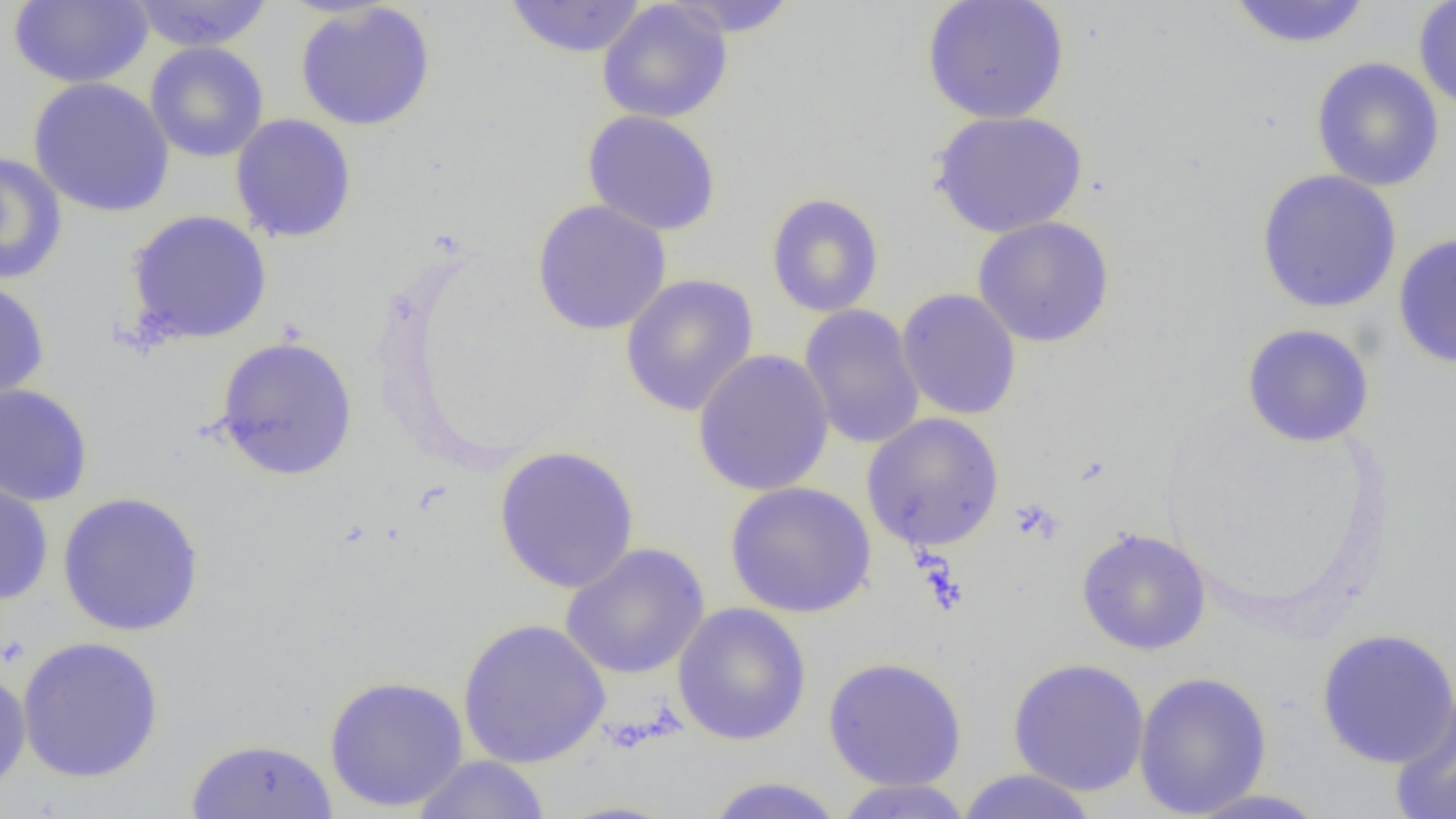

Summary:
  - Coordinate format: approximate bounding boxes as named x1/y1/x2/y2 corners in pixels
  - Platelet locations: (x1=1009, y1=498, x2=1064, y2=544)
  - Uninfected red blood cell locations: (x1=128, y1=0, x2=275, y2=52), (x1=663, y1=0, x2=801, y2=37), (x1=921, y1=0, x2=1070, y2=125), (x1=1223, y1=0, x2=1375, y2=49), (x1=1412, y1=0, x2=1456, y2=113), (x1=9, y1=1, x2=153, y2=88), (x1=503, y1=1, x2=649, y2=58), (x1=596, y1=1, x2=733, y2=124), (x1=294, y1=2, x2=437, y2=131), (x1=144, y1=42, x2=269, y2=163), (x1=1310, y1=56, x2=1445, y2=192), (x1=27, y1=77, x2=175, y2=218), (x1=929, y1=109, x2=1089, y2=238), (x1=582, y1=110, x2=722, y2=236), (x1=230, y1=114, x2=358, y2=243), (x1=0, y1=151, x2=67, y2=286), (x1=1255, y1=169, x2=1402, y2=314), (x1=765, y1=193, x2=885, y2=318), (x1=531, y1=200, x2=672, y2=336), (x1=125, y1=210, x2=273, y2=346), (x1=972, y1=216, x2=1115, y2=348), (x1=1392, y1=234, x2=1456, y2=369), (x1=620, y1=273, x2=759, y2=417), (x1=0, y1=278, x2=50, y2=406), (x1=896, y1=288, x2=1022, y2=421), (x1=799, y1=304, x2=925, y2=450), (x1=1241, y1=324, x2=1375, y2=448), (x1=213, y1=336, x2=359, y2=481), (x1=692, y1=348, x2=835, y2=497), (x1=0, y1=382, x2=94, y2=507), (x1=861, y1=412, x2=1005, y2=552), (x1=493, y1=445, x2=640, y2=594), (x1=0, y1=472, x2=54, y2=606), (x1=724, y1=481, x2=877, y2=618), (x1=57, y1=491, x2=205, y2=637), (x1=1076, y1=527, x2=1211, y2=655), (x1=559, y1=542, x2=711, y2=681), (x1=672, y1=602, x2=812, y2=746), (x1=456, y1=617, x2=612, y2=769), (x1=1316, y1=628, x2=1456, y2=769), (x1=16, y1=635, x2=165, y2=784), (x1=823, y1=656, x2=968, y2=791), (x1=1007, y1=657, x2=1150, y2=797), (x1=0, y1=667, x2=32, y2=796), (x1=1133, y1=670, x2=1272, y2=817), (x1=324, y1=674, x2=468, y2=812), (x1=1390, y1=690, x2=1456, y2=819), (x1=184, y1=737, x2=338, y2=818), (x1=410, y1=755, x2=553, y2=819), (x1=955, y1=769, x2=1100, y2=819), (x1=702, y1=775, x2=847, y2=819), (x1=832, y1=779, x2=975, y2=818), (x1=1180, y1=788, x2=1333, y2=818)
  - Slide-level diagnosis: no evidence of blood parasites
  - Field of view: single
  - Modality: light microscopy
  - Magnification: 1000x
  - Image size: 1456×819 pixels
  - Preparation: thin blood film